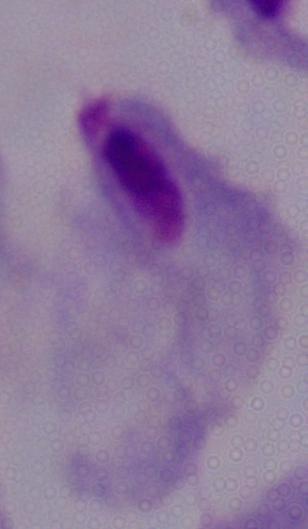

modality = photomicrograph
identification = trichomonad
magnification = 1000x